State which parasite is depicted.
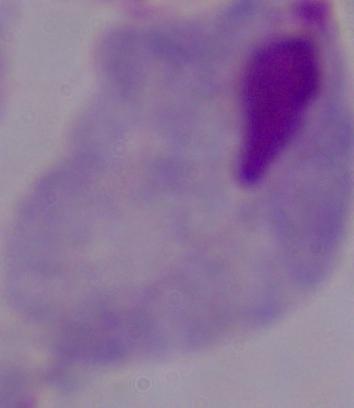
This is a trichomonad.

Summary:
  - Magnification: 1000x
  - Modality: micrograph